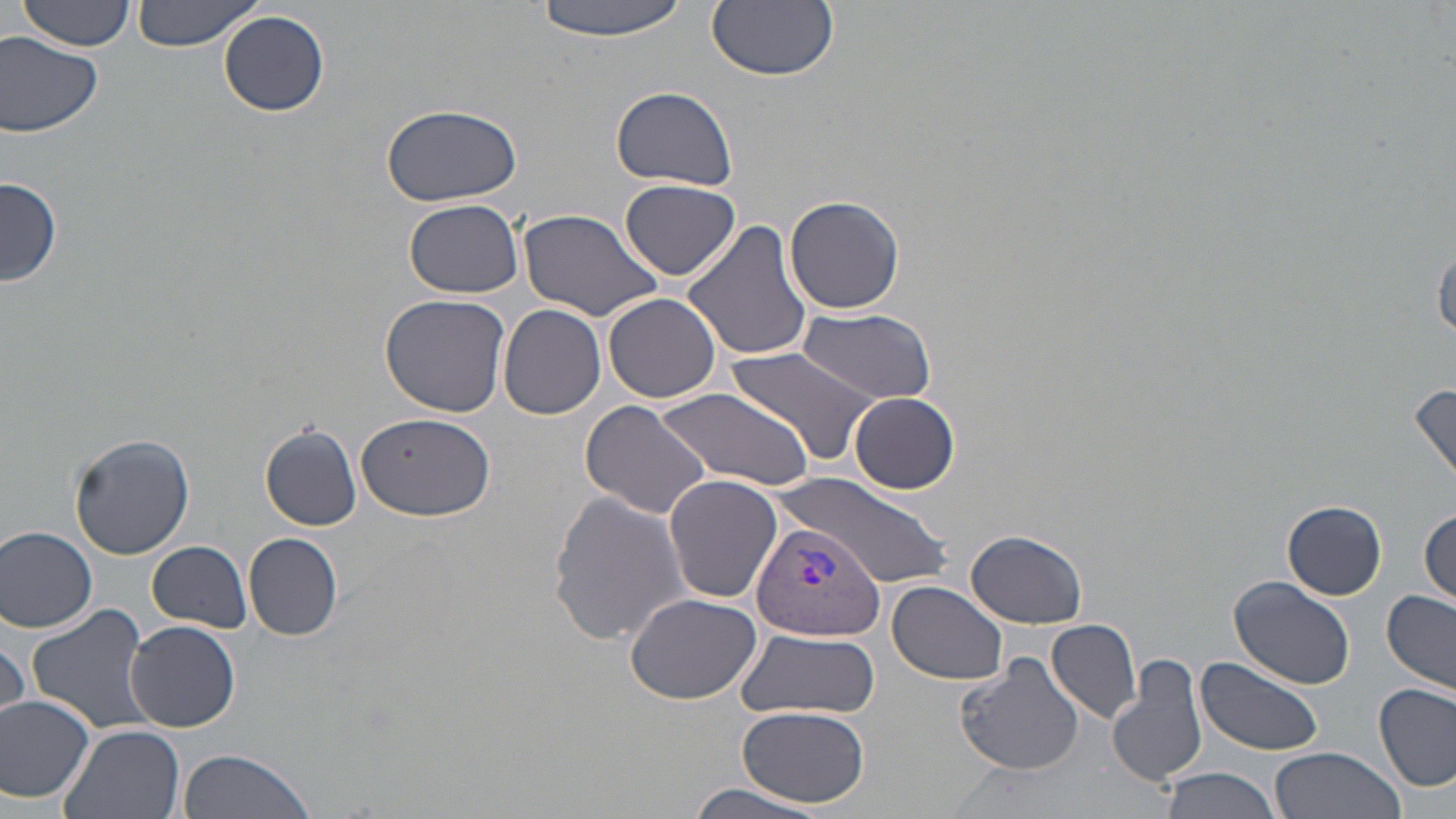
slide-level diagnosis = Plasmodium vivax
preparation = thin blood smear
field of view = single
uninfected red blood cell locations = approximate bounding boxes as (x1, y1, x2, y2) in pixels: (132, 0, 262, 51), (532, 0, 692, 41), (19, 1, 137, 52), (707, 1, 838, 82), (219, 10, 329, 117), (1, 31, 103, 136), (612, 85, 738, 191), (380, 103, 522, 207), (1, 175, 61, 288), (619, 181, 743, 283), (784, 194, 905, 314), (406, 199, 523, 298), (517, 208, 663, 321), (683, 218, 813, 363), (1433, 243, 1456, 339), (379, 293, 511, 418), (602, 293, 722, 404), (497, 304, 605, 419), (795, 310, 936, 404), (728, 343, 879, 467), (1408, 377, 1456, 487), (650, 383, 818, 492), (848, 392, 960, 494), (579, 400, 714, 520), (357, 413, 494, 523), (261, 423, 363, 532), (69, 432, 195, 560), (778, 473, 948, 584), (663, 474, 782, 604), (548, 488, 694, 648), (1282, 501, 1387, 599), (1419, 505, 1455, 607), (0, 525, 99, 634), (965, 529, 1087, 628), (244, 532, 344, 640), (147, 541, 252, 632), (1228, 576, 1355, 689), (887, 581, 1009, 685), (1383, 590, 1456, 693), (624, 592, 763, 705), (26, 605, 154, 736), (125, 620, 241, 732), (1046, 620, 1142, 725), (735, 629, 880, 719), (954, 650, 1084, 776), (1108, 652, 1209, 791), (1196, 657, 1325, 756), (1375, 682, 1455, 793), (0, 694, 97, 804), (738, 706, 870, 809), (59, 723, 186, 819), (1269, 746, 1407, 819), (177, 748, 317, 819), (1158, 767, 1281, 819), (682, 779, 830, 817)
modality = optical microscopy
Plasmodium vivax-infected red blood cell locations = approximate bounding boxes as (x1, y1, x2, y2) in pixels: (751, 519, 887, 640)
stain = May-Grünwald-Giemsa
image size = 1456×819 pixels
magnification = 1000x